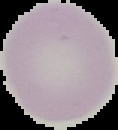
Summary:
  - Image type: segmented cell region with the area outside set to black
  - Preparation: thin blood smear
  - Malaria status: uninfected
  - Image size: 118×130 pixels